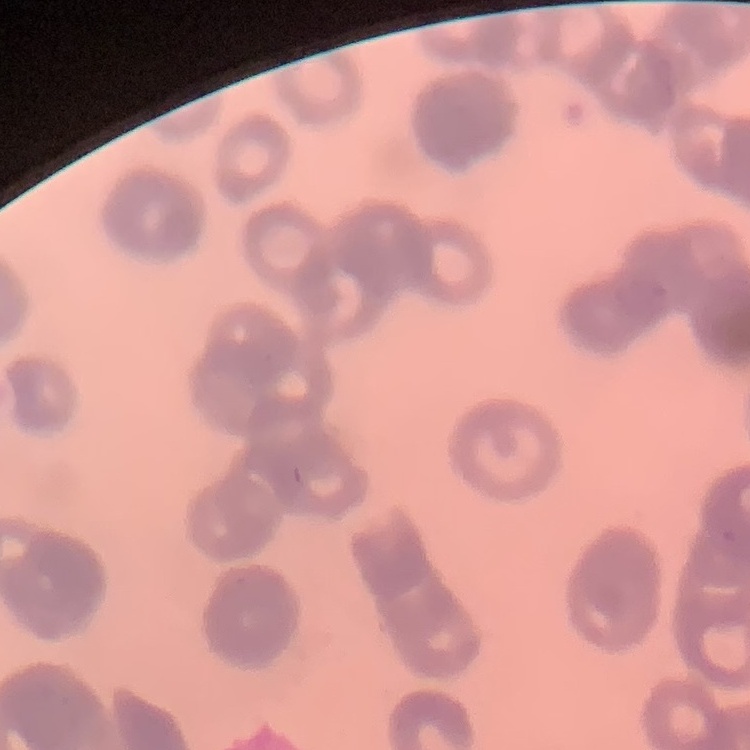

The red blood cells show rouleaux formation. Field's or Giemsa stain. Square crop of a larger photomicrograph. Thin peripheral smear.